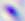
400x magnification. Toxoplasma gondii is shown. Photomicrograph.